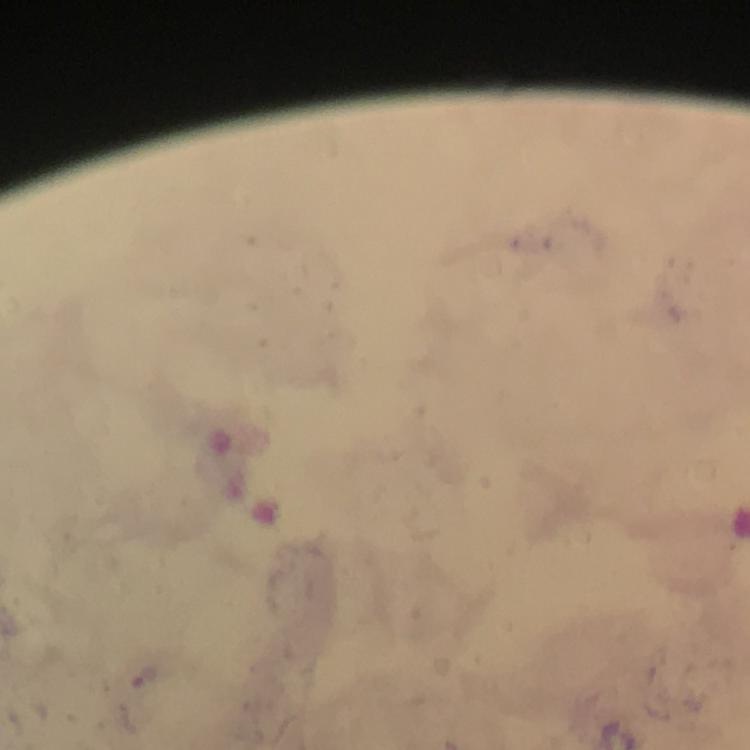

{
  "capture": "smartphone photograph through a microscope",
  "stain": "Giemsa",
  "immersion_oil": "applied",
  "malaria_parasite_locations": "approximate object centers, in pixels from the top-left corner: (x=145, y=680)",
  "magnification": "100x",
  "cropped_from": "a single field of view",
  "image_size": "750×750 pixels",
  "preparation": "thick smear",
  "context": "from a malaria diagnostic workup"
}